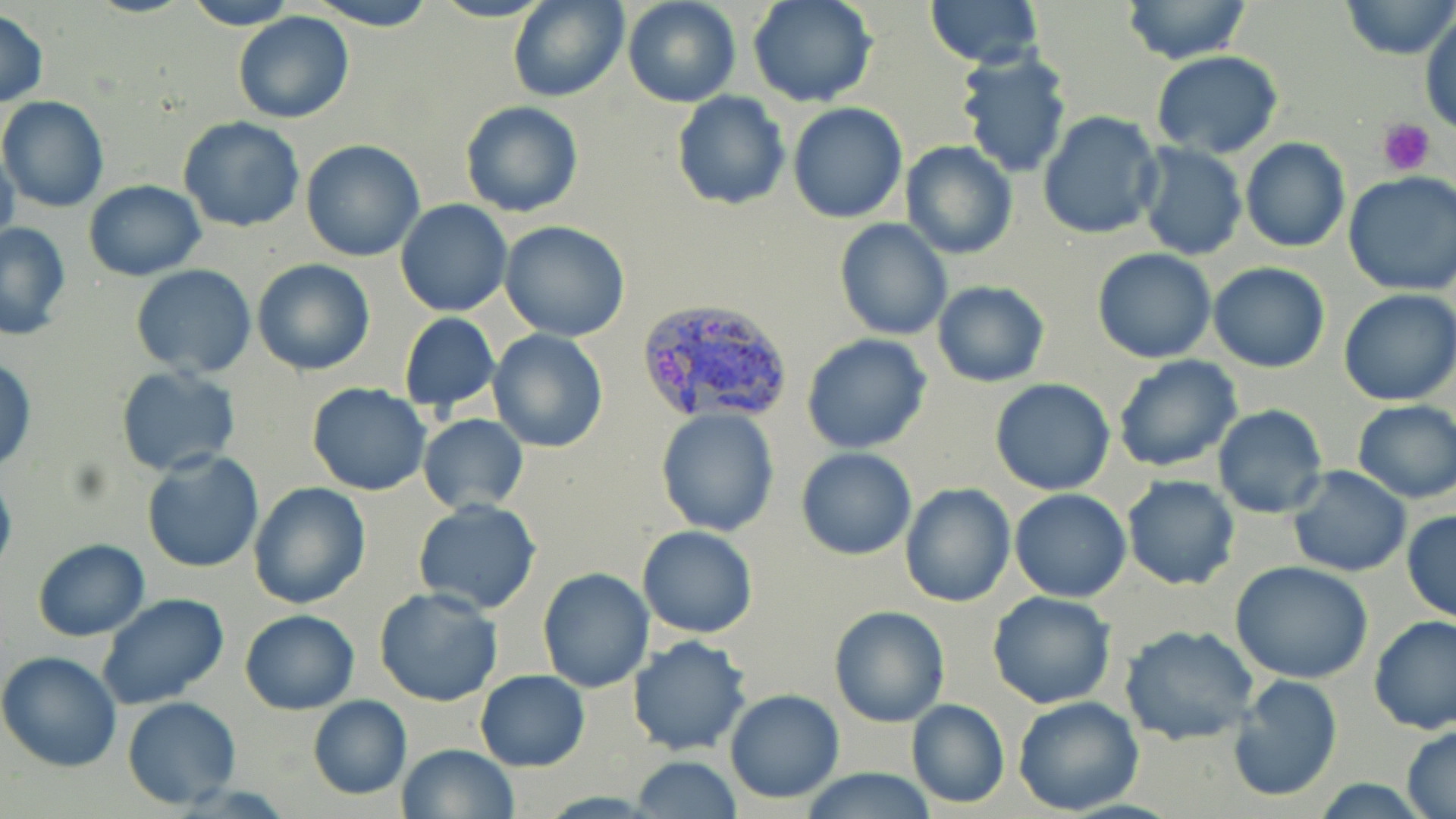 Approximate bounding boxes as [x1, y1, x2, y2] in pixels. Uninfected red blood cell locations: [183, 0, 296, 30], [305, 0, 439, 31], [509, 0, 629, 103], [622, 0, 740, 108], [748, 0, 876, 108], [925, 0, 1043, 67], [1118, 0, 1254, 65], [1341, 0, 1454, 60], [0, 7, 47, 108], [232, 12, 354, 124], [1420, 12, 1455, 132], [955, 49, 1073, 177], [1152, 52, 1283, 159], [670, 90, 791, 212], [0, 96, 109, 212], [460, 100, 584, 219], [786, 102, 907, 223], [1038, 111, 1164, 241], [177, 116, 306, 234], [1240, 138, 1350, 253], [299, 139, 426, 261], [900, 141, 1018, 259], [1135, 143, 1247, 260], [0, 148, 20, 260], [1342, 171, 1456, 296], [83, 180, 207, 280], [395, 201, 511, 317], [834, 217, 953, 341], [499, 219, 631, 342], [0, 222, 72, 340], [1093, 248, 1216, 363], [252, 258, 376, 377], [1208, 262, 1330, 373], [131, 265, 257, 378], [931, 282, 1050, 387], [1338, 289, 1456, 405], [398, 312, 501, 414], [487, 329, 609, 453], [802, 334, 932, 455], [1113, 356, 1242, 474], [0, 359, 37, 474], [114, 366, 240, 476], [989, 379, 1115, 496], [307, 381, 432, 496], [1351, 400, 1456, 504], [1211, 404, 1328, 520], [656, 408, 782, 537], [418, 413, 528, 514], [141, 449, 266, 572], [796, 449, 918, 560], [1286, 466, 1412, 577], [0, 470, 16, 582], [1120, 474, 1241, 590], [248, 482, 371, 609], [900, 483, 1014, 608], [1010, 489, 1130, 602], [411, 498, 542, 615], [1402, 509, 1456, 625], [638, 525, 758, 638], [32, 538, 150, 641], [1230, 561, 1374, 684], [536, 567, 655, 693], [373, 587, 504, 706], [987, 591, 1117, 710], [97, 594, 229, 712], [829, 605, 949, 727], [240, 609, 360, 713], [1368, 614, 1456, 735], [1120, 625, 1260, 747], [625, 635, 751, 756], [0, 650, 122, 773], [475, 669, 589, 773], [1225, 675, 1343, 804], [724, 689, 846, 804], [308, 695, 412, 800], [1011, 695, 1144, 815], [122, 696, 242, 808], [906, 699, 1010, 809], [1401, 724, 1456, 818], [397, 744, 518, 818], [630, 757, 745, 817], [797, 768, 938, 819]. Platelet locations: [1380, 119, 1436, 176]. Plasmodium vivax-infected red blood cell locations: [637, 296, 796, 424]. Slide-level diagnosis: Plasmodium vivax. One field of a larger specimen. Light microscopy. Image is 1456×819 pixels. May-Grünwald-Giemsa-stained preparation. 1000x magnification. Thin blood film.